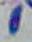

modality = micrograph
identification = Toxoplasma gondii
magnification = 1000x